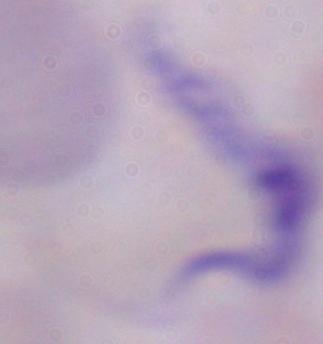
Summary:
  - Modality: photomicrograph
  - Identification: trypanosome
  - Magnification: 1000x